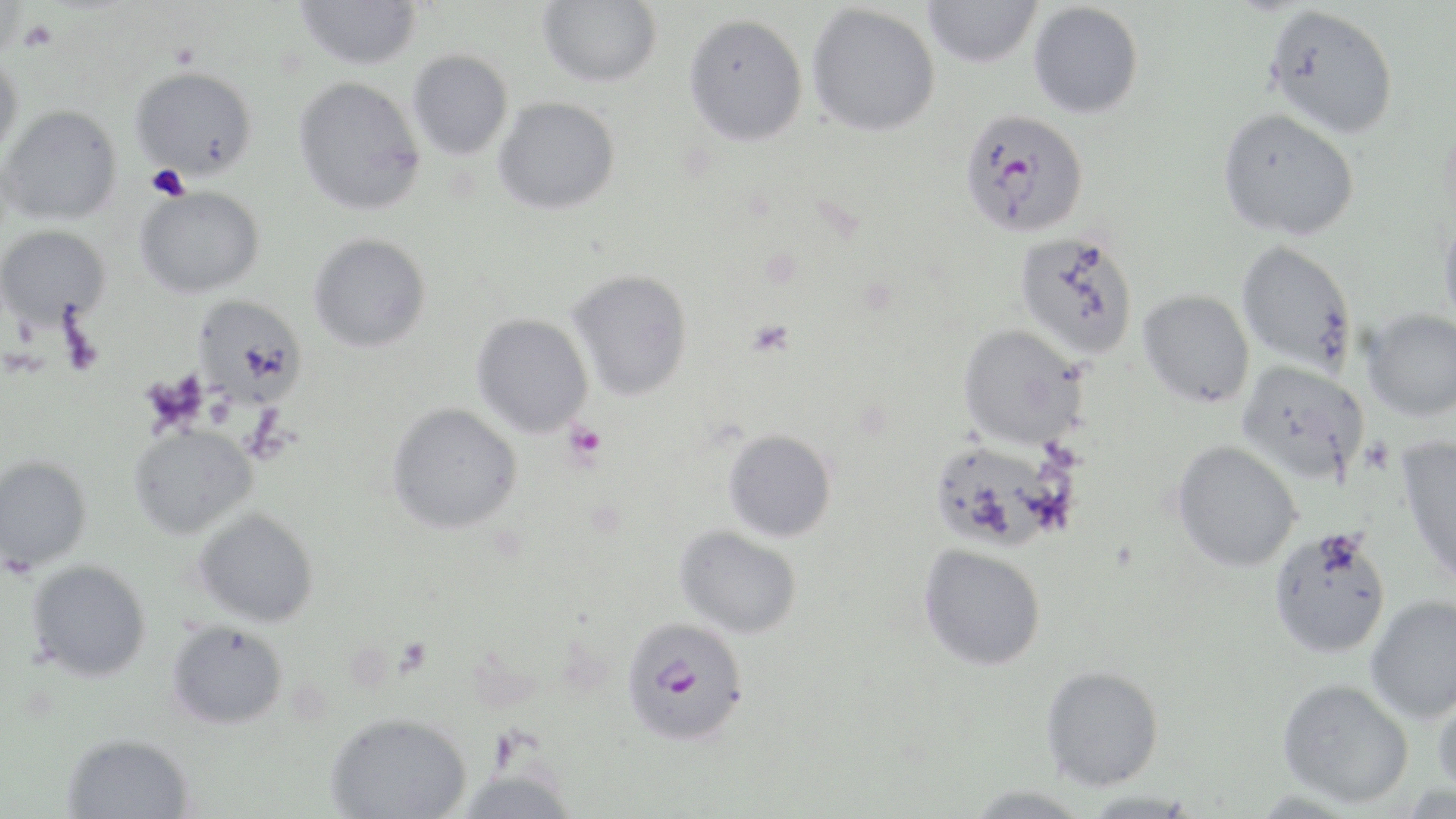
Summary:
  - Coordinate format: approximate bounding boxes as (x1, y1, x2, y2) in pixels
  - Plasmodium falciparum-infected red blood cell locations: (959, 108, 1089, 238), (620, 617, 751, 744)
  - Uninfected red blood cell locations: (296, 0, 422, 70), (537, 0, 662, 87), (922, 0, 1042, 68), (0, 1, 27, 61), (1028, 2, 1144, 119), (807, 3, 940, 137), (1264, 4, 1400, 137), (683, 13, 808, 147), (408, 49, 513, 160), (0, 53, 23, 159), (130, 66, 258, 180), (293, 76, 425, 215), (493, 97, 620, 215), (1, 105, 123, 225), (1217, 108, 1360, 240), (134, 186, 265, 298), (1439, 214, 1456, 331), (0, 225, 110, 329), (1013, 230, 1140, 360), (308, 234, 431, 353), (1235, 241, 1359, 374), (567, 269, 693, 401), (1137, 290, 1255, 408), (193, 296, 308, 407), (1363, 309, 1456, 421), (471, 314, 593, 438), (957, 324, 1088, 449), (1236, 360, 1369, 483), (386, 403, 523, 535), (128, 424, 258, 539), (723, 429, 837, 543), (1397, 436, 1456, 586), (929, 440, 1065, 552), (1170, 440, 1302, 572), (0, 456, 92, 571), (193, 508, 320, 627), (675, 525, 802, 638), (1268, 528, 1391, 658), (918, 544, 1046, 670), (26, 561, 151, 682), (1365, 595, 1456, 723), (166, 620, 288, 729), (1040, 665, 1164, 791), (1277, 678, 1414, 808), (1433, 687, 1456, 799), (325, 711, 471, 819), (61, 733, 195, 819), (453, 765, 579, 818), (963, 785, 1094, 819), (1081, 792, 1201, 818)
  - Platelet locations: (18, 19, 58, 52), (745, 319, 795, 358), (564, 422, 607, 464)
  - Slide-level diagnosis: Plasmodium falciparum
  - Preparation: thin blood smear
  - Stain: May-Grünwald-Giemsa
  - Image size: 1456×819 pixels
  - Modality: optical microscopy
  - Field of view: single
  - Magnification: 1000x